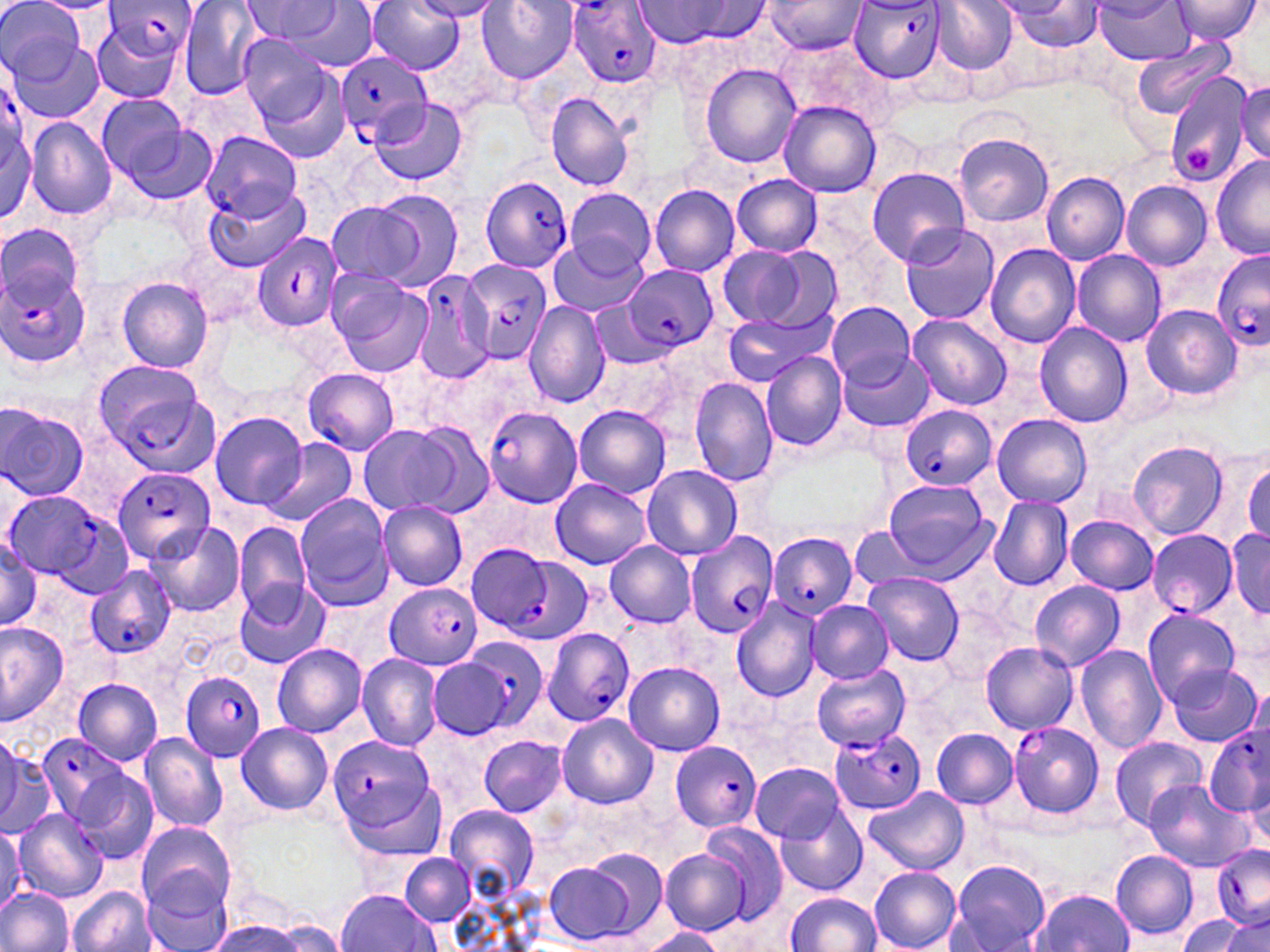 Approximate bounding boxes as named x1/y1/x2/y2 corners in pixels. Uninfected red blood cell locations: (x1=1, y1=0, x2=86, y2=84), (x1=633, y1=0, x2=749, y2=48), (x1=765, y1=0, x2=867, y2=55), (x1=932, y1=0, x2=1017, y2=74), (x1=1091, y1=0, x2=1195, y2=64), (x1=1168, y1=0, x2=1262, y2=45), (x1=177, y1=1, x2=272, y2=101), (x1=243, y1=1, x2=340, y2=45), (x1=365, y1=1, x2=465, y2=74), (x1=410, y1=1, x2=504, y2=22), (x1=476, y1=1, x2=579, y2=83), (x1=1001, y1=2, x2=1105, y2=51), (x1=279, y1=3, x2=381, y2=76), (x1=90, y1=17, x2=184, y2=103), (x1=236, y1=32, x2=337, y2=128), (x1=8, y1=35, x2=103, y2=123), (x1=781, y1=38, x2=893, y2=127), (x1=1131, y1=41, x2=1235, y2=119), (x1=698, y1=64, x2=801, y2=167), (x1=1164, y1=73, x2=1253, y2=189), (x1=1235, y1=80, x2=1269, y2=163), (x1=95, y1=92, x2=199, y2=191), (x1=546, y1=93, x2=635, y2=192), (x1=370, y1=98, x2=467, y2=186), (x1=778, y1=100, x2=880, y2=198), (x1=1, y1=113, x2=37, y2=226), (x1=27, y1=119, x2=116, y2=219), (x1=953, y1=133, x2=1054, y2=226), (x1=1211, y1=157, x2=1270, y2=260), (x1=865, y1=167, x2=970, y2=265), (x1=1042, y1=172, x2=1129, y2=264), (x1=731, y1=175, x2=823, y2=255), (x1=1121, y1=180, x2=1212, y2=270), (x1=650, y1=185, x2=739, y2=276), (x1=563, y1=187, x2=659, y2=272), (x1=205, y1=189, x2=310, y2=271), (x1=373, y1=189, x2=466, y2=291), (x1=326, y1=202, x2=419, y2=285), (x1=1, y1=221, x2=83, y2=309), (x1=899, y1=224, x2=1000, y2=326), (x1=550, y1=238, x2=645, y2=316), (x1=986, y1=243, x2=1081, y2=347), (x1=716, y1=244, x2=837, y2=333), (x1=1071, y1=250, x2=1166, y2=347), (x1=117, y1=277, x2=215, y2=373), (x1=329, y1=277, x2=435, y2=377), (x1=825, y1=301, x2=915, y2=386), (x1=524, y1=302, x2=610, y2=410), (x1=589, y1=302, x2=670, y2=368), (x1=1140, y1=304, x2=1240, y2=401), (x1=721, y1=313, x2=828, y2=386), (x1=906, y1=314, x2=1013, y2=410), (x1=1034, y1=322, x2=1133, y2=428), (x1=840, y1=350, x2=933, y2=432), (x1=761, y1=353, x2=848, y2=452), (x1=303, y1=368, x2=399, y2=454), (x1=691, y1=379, x2=781, y2=488), (x1=1, y1=404, x2=89, y2=502), (x1=574, y1=405, x2=671, y2=498), (x1=211, y1=413, x2=308, y2=511), (x1=992, y1=414, x2=1092, y2=507), (x1=402, y1=423, x2=495, y2=517), (x1=357, y1=425, x2=464, y2=517), (x1=263, y1=437, x2=358, y2=527), (x1=1128, y1=440, x2=1230, y2=541), (x1=1245, y1=459, x2=1269, y2=545), (x1=643, y1=466, x2=742, y2=560), (x1=550, y1=479, x2=651, y2=569), (x1=884, y1=479, x2=992, y2=577), (x1=294, y1=495, x2=393, y2=611), (x1=989, y1=497, x2=1072, y2=592), (x1=378, y1=502, x2=469, y2=591), (x1=1065, y1=515, x2=1159, y2=594), (x1=147, y1=522, x2=245, y2=618), (x1=235, y1=522, x2=311, y2=615), (x1=852, y1=527, x2=928, y2=595), (x1=1228, y1=529, x2=1270, y2=615), (x1=0, y1=536, x2=41, y2=634), (x1=605, y1=541, x2=697, y2=627), (x1=864, y1=572, x2=964, y2=667), (x1=234, y1=580, x2=328, y2=670), (x1=1029, y1=580, x2=1124, y2=672), (x1=807, y1=601, x2=894, y2=682), (x1=731, y1=602, x2=822, y2=701), (x1=1142, y1=607, x2=1240, y2=704), (x1=0, y1=621, x2=69, y2=725), (x1=980, y1=642, x2=1078, y2=734), (x1=272, y1=643, x2=367, y2=737), (x1=1075, y1=645, x2=1167, y2=754), (x1=358, y1=654, x2=443, y2=751), (x1=428, y1=659, x2=511, y2=739), (x1=624, y1=663, x2=725, y2=755), (x1=1167, y1=663, x2=1264, y2=748), (x1=73, y1=678, x2=163, y2=764), (x1=556, y1=714, x2=658, y2=808), (x1=235, y1=723, x2=333, y2=815), (x1=931, y1=728, x2=1019, y2=807), (x1=137, y1=732, x2=225, y2=832), (x1=0, y1=735, x2=53, y2=836), (x1=478, y1=735, x2=567, y2=816), (x1=1108, y1=735, x2=1208, y2=831), (x1=751, y1=762, x2=846, y2=843), (x1=77, y1=773, x2=158, y2=863), (x1=1143, y1=781, x2=1251, y2=873), (x1=864, y1=788, x2=970, y2=875), (x1=445, y1=805, x2=538, y2=895), (x1=774, y1=806, x2=866, y2=894), (x1=11, y1=807, x2=109, y2=903), (x1=137, y1=822, x2=235, y2=913), (x1=699, y1=822, x2=789, y2=923), (x1=0, y1=829, x2=24, y2=907), (x1=660, y1=849, x2=749, y2=936), (x1=1110, y1=850, x2=1199, y2=941), (x1=400, y1=852, x2=474, y2=925), (x1=544, y1=858, x2=648, y2=947), (x1=948, y1=861, x2=1051, y2=951), (x1=869, y1=867, x2=961, y2=951), (x1=140, y1=873, x2=233, y2=950), (x1=67, y1=887, x2=158, y2=952), (x1=334, y1=888, x2=440, y2=951), (x1=0, y1=889, x2=73, y2=952), (x1=1031, y1=889, x2=1135, y2=952), (x1=784, y1=893, x2=881, y2=951), (x1=1179, y1=914, x2=1252, y2=952), (x1=1218, y1=915, x2=1270, y2=952), (x1=209, y1=917, x2=299, y2=952), (x1=267, y1=917, x2=351, y2=951), (x1=638, y1=928, x2=725, y2=952). Plasmodium falciparum-infected red blood cell locations: (x1=569, y1=0, x2=660, y2=87), (x1=105, y1=1, x2=200, y2=61), (x1=853, y1=1, x2=951, y2=80), (x1=335, y1=51, x2=431, y2=145), (x1=1, y1=82, x2=27, y2=169), (x1=201, y1=132, x2=303, y2=220), (x1=480, y1=177, x2=574, y2=272), (x1=251, y1=230, x2=343, y2=333), (x1=1213, y1=248, x2=1270, y2=351), (x1=461, y1=260, x2=551, y2=362), (x1=0, y1=262, x2=89, y2=374), (x1=626, y1=266, x2=718, y2=352), (x1=412, y1=269, x2=497, y2=384), (x1=92, y1=359, x2=219, y2=471), (x1=898, y1=405, x2=997, y2=490), (x1=483, y1=406, x2=583, y2=507), (x1=113, y1=468, x2=217, y2=563), (x1=7, y1=491, x2=123, y2=591), (x1=686, y1=529, x2=779, y2=638), (x1=1147, y1=530, x2=1238, y2=615), (x1=767, y1=532, x2=858, y2=619), (x1=467, y1=543, x2=581, y2=643), (x1=86, y1=565, x2=177, y2=659), (x1=383, y1=583, x2=481, y2=669), (x1=542, y1=628, x2=635, y2=727), (x1=447, y1=638, x2=547, y2=736), (x1=812, y1=666, x2=911, y2=750), (x1=181, y1=672, x2=268, y2=761), (x1=1009, y1=722, x2=1105, y2=819), (x1=831, y1=727, x2=926, y2=815), (x1=1204, y1=727, x2=1268, y2=822), (x1=35, y1=732, x2=129, y2=826), (x1=327, y1=734, x2=437, y2=834), (x1=670, y1=740, x2=761, y2=831), (x1=1212, y1=843, x2=1270, y2=926). Platelet locations: (x1=1183, y1=146, x2=1217, y2=174). Slide-level diagnosis: Plasmodium falciparum. Image is 1270×952 pixels. 1000x magnification. Thin blood film. May-Grünwald-Giemsa stain. One field of a larger specimen. Light microscopy.